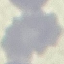
Summary:
  - Result: negative for malaria parasites
  - Capture: smartphone through the microscope eyepiece
  - Preparation: thin blood smear
  - Stain: Giemsa
  - Image type: automatically extracted cell patch, resized to 64 × 64 pixels